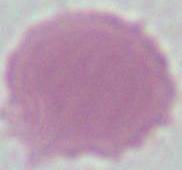
magnification = 1000x
identification = erythrocyte
modality = photomicrograph